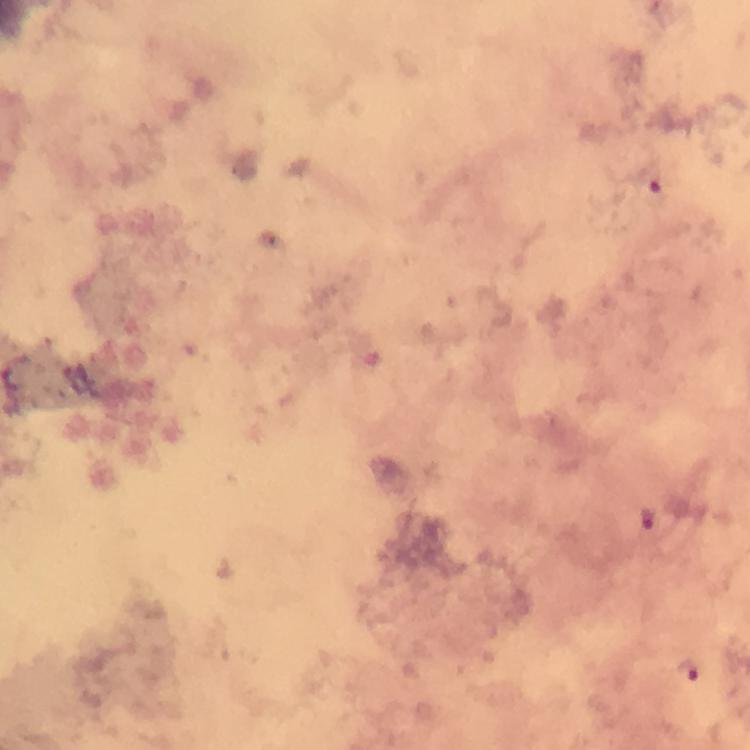

Approximate centers as [x, y] in pixels.
Summary:
  - Plasmodium parasite locations: [647, 519], [689, 670]
  - Stain: Giemsa
  - Cropped from: a single field of view
  - Image size: 750×750 pixels
  - Context: from a malaria diagnostic workup
  - Magnification: 100x
  - Immersion oil: applied
  - Preparation: thick blood smear
  - Capture: smartphone mounted on the microscope